Assess this cell for malaria.
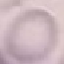

Uninfected.

Summary:
  - Preparation: thin smear
  - Image type: automatically extracted cell patch, resized to 64 × 64 pixels
  - Stain: Giemsa
  - Capture: smartphone camera at the microscope eyepiece